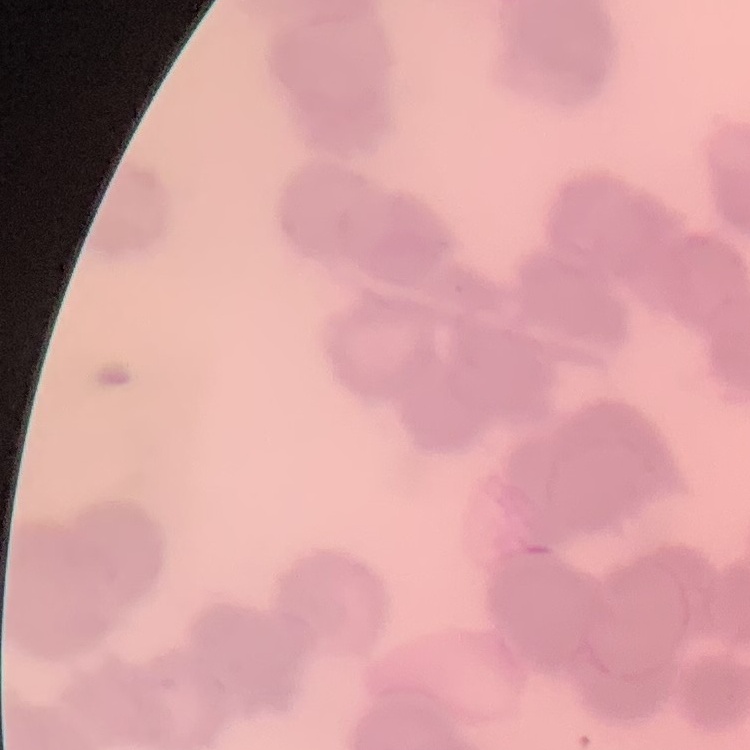
Summary:
  - Red blood cell morphology: rouleaux formation
  - Stain: Field's or Giemsa
  - Image type: one tile cut from a larger photomicrograph
  - Preparation: thin blood film